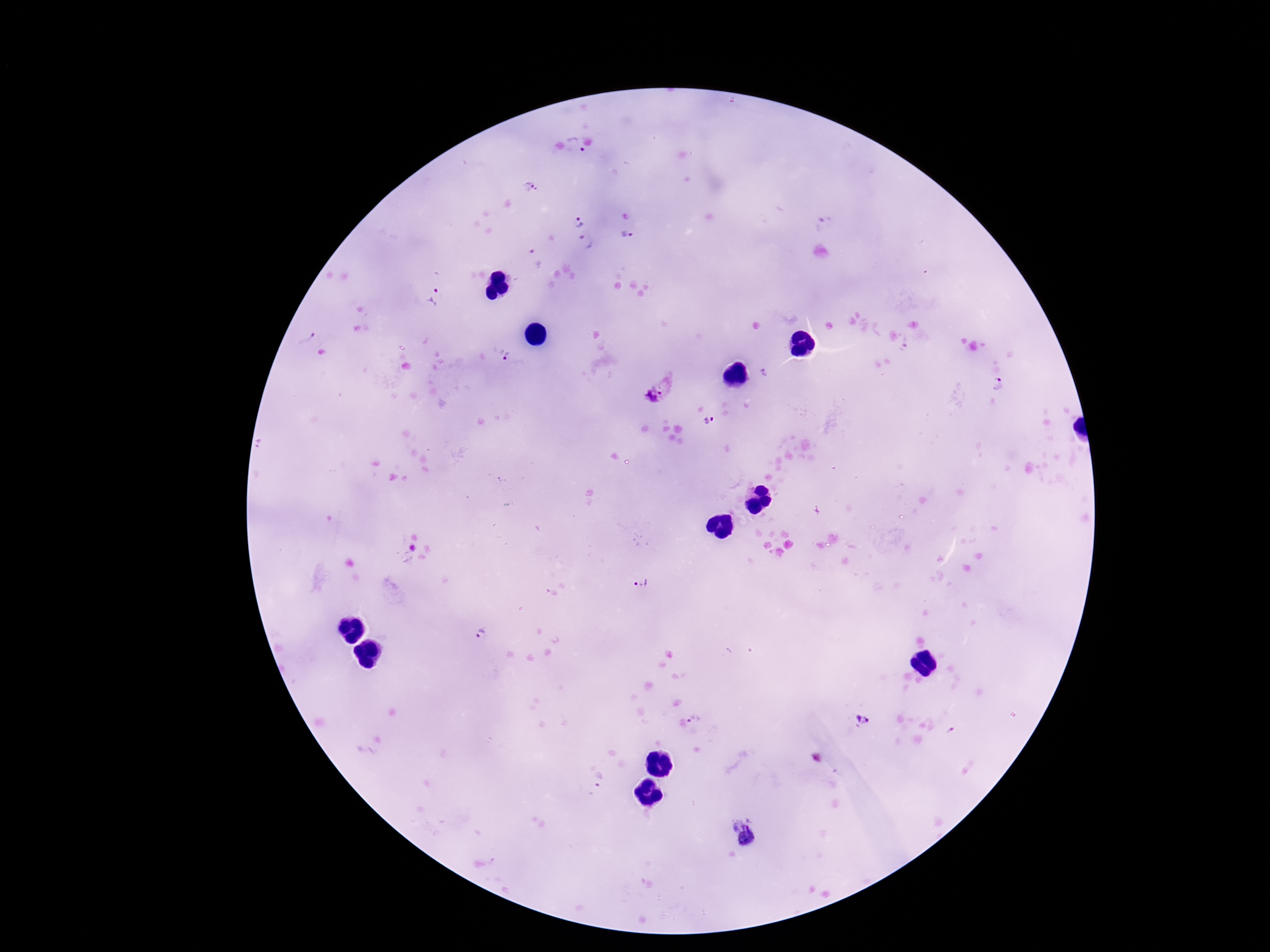
Approximate centers as [x, y] in pixels. Plasmodium parasite locations: [573, 144], [530, 186], [579, 223], [823, 225], [626, 234], [586, 242], [534, 258], [435, 298], [304, 334], [501, 353], [765, 372], [1001, 384], [657, 392], [712, 422], [644, 586], [483, 636], [697, 717], [862, 719], [952, 730], [601, 779], [747, 838]. Image is 1270×952 pixels. Patient malaria status: infected. Thick peripheral-blood smear. Photographed through the microscope eyepiece with a smartphone camera. Giemsa stain. 100x magnification. One field from this slide.